Classify this cell by malaria status.
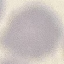
Uninfected.

Summary:
  - Image type: automatically extracted cell patch, resized to 64 × 64 pixels
  - Preparation: thin smear
  - Capture: smartphone camera at the microscope eyepiece
  - Stain: Giemsa